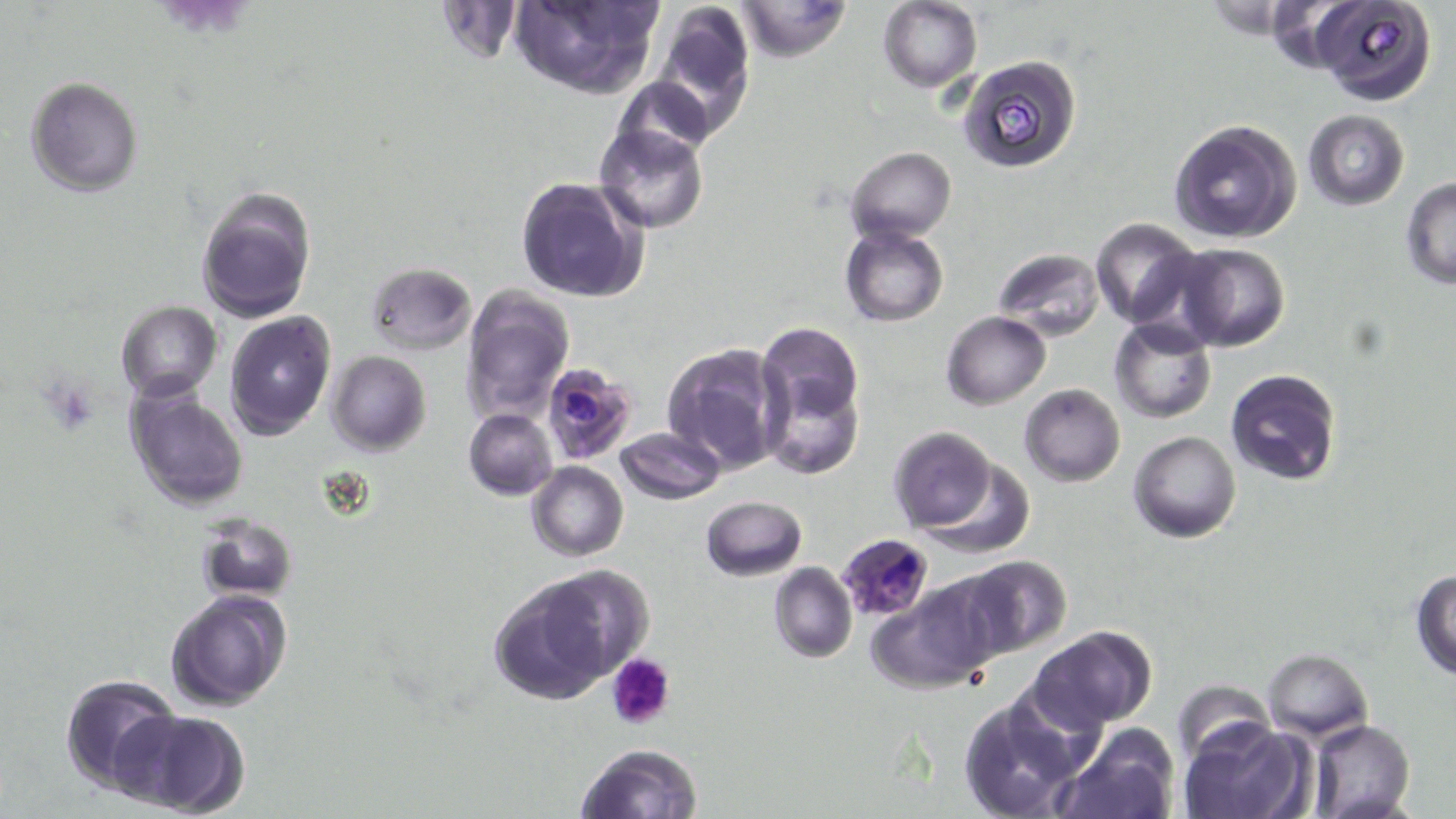

Approximate bounding boxes as (x1, y1, x2, y2) in pixels. Plasmodium falciparum-infected red blood cell locations: (540, 361, 638, 465), (843, 534, 938, 623). Uninfected red blood cell locations: (508, 0, 663, 100), (1309, 0, 1436, 104), (647, 1, 757, 139), (734, 1, 852, 59), (877, 2, 982, 91), (959, 55, 1081, 174), (25, 76, 144, 197), (612, 76, 715, 163), (1303, 111, 1409, 210), (1167, 119, 1301, 245), (594, 124, 707, 234), (847, 147, 957, 243), (516, 178, 648, 303), (1400, 179, 1456, 288), (195, 185, 316, 323), (1091, 218, 1204, 328), (840, 223, 949, 328), (1172, 243, 1290, 351), (993, 248, 1104, 339), (366, 261, 477, 355), (460, 285, 574, 424), (115, 300, 223, 401), (225, 311, 337, 440), (941, 311, 1051, 408), (1110, 318, 1217, 424), (756, 329, 866, 481), (662, 343, 788, 474), (326, 351, 431, 456), (1224, 368, 1342, 485), (1018, 383, 1126, 486), (125, 388, 249, 510), (464, 408, 558, 499), (616, 426, 724, 504), (887, 427, 996, 533), (1128, 431, 1242, 543), (916, 458, 1036, 560), (526, 461, 628, 561), (701, 494, 807, 582), (195, 512, 298, 601), (956, 555, 1071, 659), (768, 562, 857, 664), (1410, 570, 1456, 679), (488, 572, 628, 705), (870, 578, 1002, 692), (165, 589, 292, 712), (1030, 625, 1157, 731), (1263, 648, 1373, 740), (59, 673, 181, 796), (1171, 681, 1273, 764), (958, 698, 1083, 819), (116, 709, 248, 817), (1180, 718, 1313, 819), (1307, 719, 1414, 819), (1055, 727, 1180, 819), (575, 743, 704, 819). Platelet locations: (44, 377, 101, 432), (607, 653, 676, 730). Slide-level diagnosis: Plasmodium falciparum. Light microscopy. 1000x magnification. Image is 1456×819 pixels. Thin blood film. May-Grünwald-Giemsa stain. Single field of view.